Name the parasite shown.
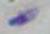

Toxoplasma gondii.

{
  "magnification": "1000x",
  "modality": "micrograph"
}